Locate every Plasmodium parasite.
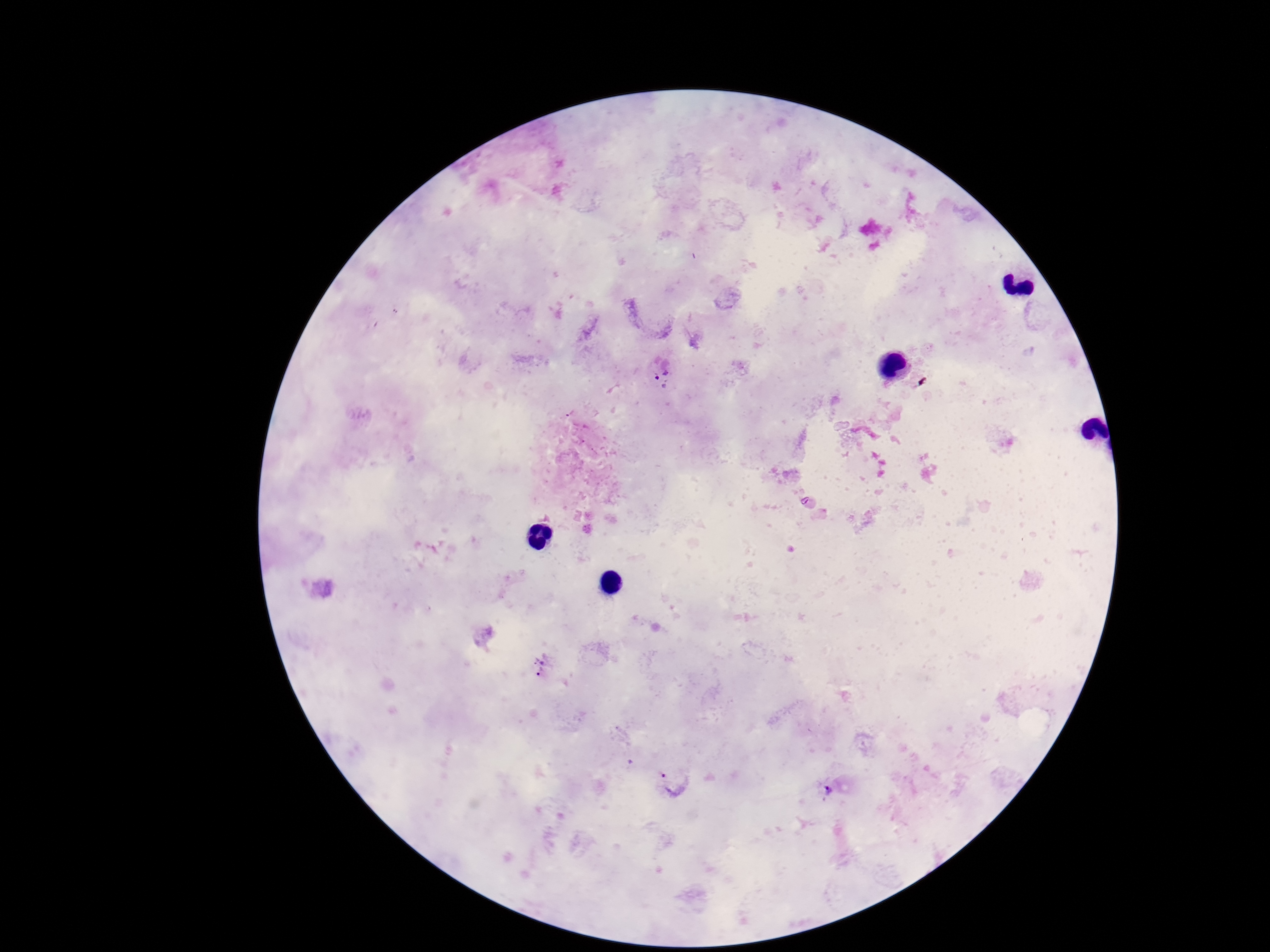
Approximate centers as {x, y} in pixels.
Plasmodium parasites: {661, 372}, {544, 666}, {674, 782}, {828, 791}.

{
  "magnification": "100x",
  "stain": "Giemsa",
  "image_size": "1270×952 pixels",
  "field_of_view": "single",
  "patient_malaria_status": "infected",
  "preparation": "thick peripheral-blood smear",
  "capture": "smartphone camera through the microscope eyepiece"
}